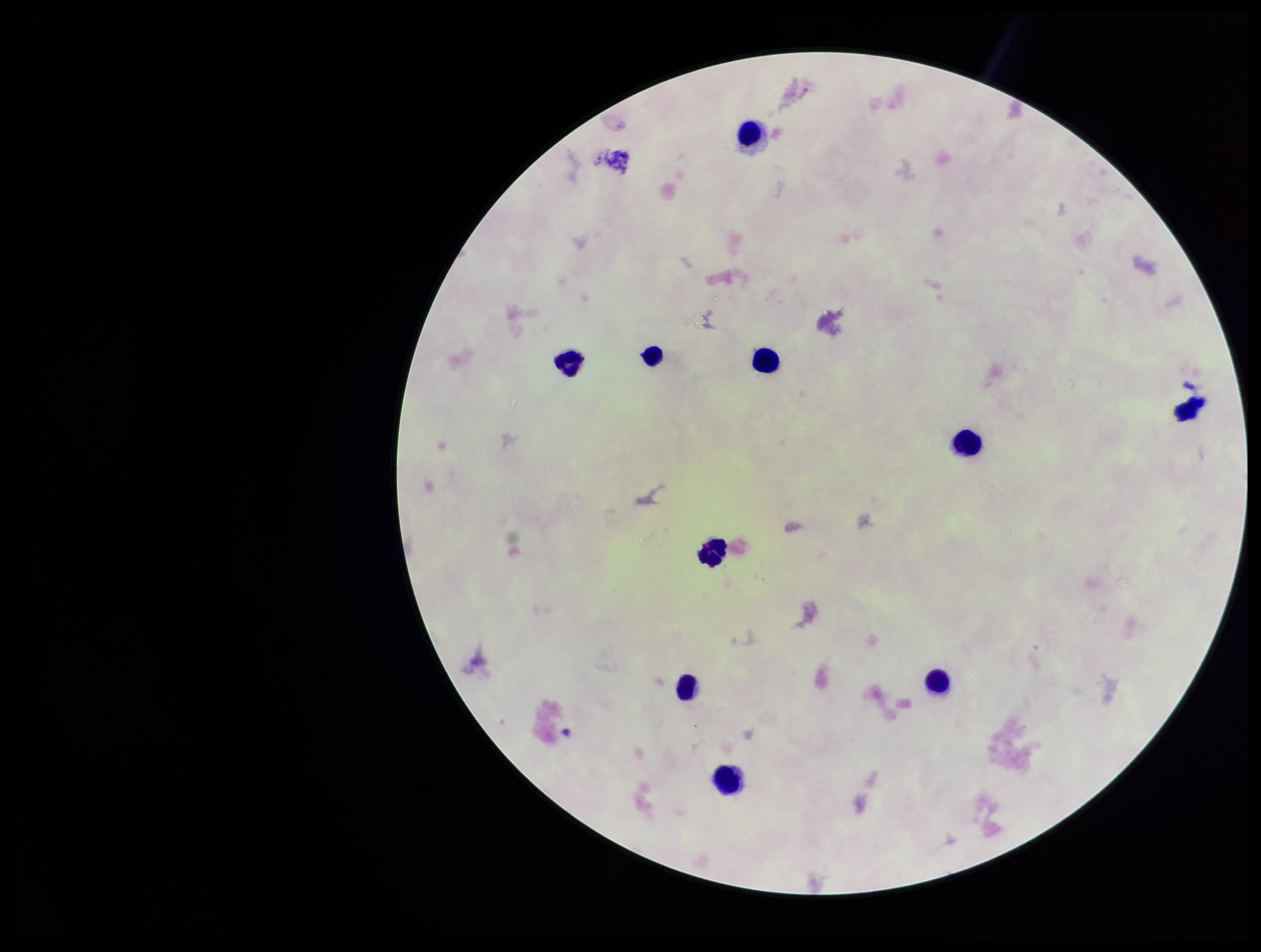 Parasite count: 0. Smartphone photograph taken through the eyepiece of a microscope. Stained with Giemsa. Leukocyte count: 10. Patient malaria status: negative. One field from this slide. Image is 1261×952 pixels. Plasmodium parasites: none detected. Preparation: thick blood smear.